Point out each leukocyte.
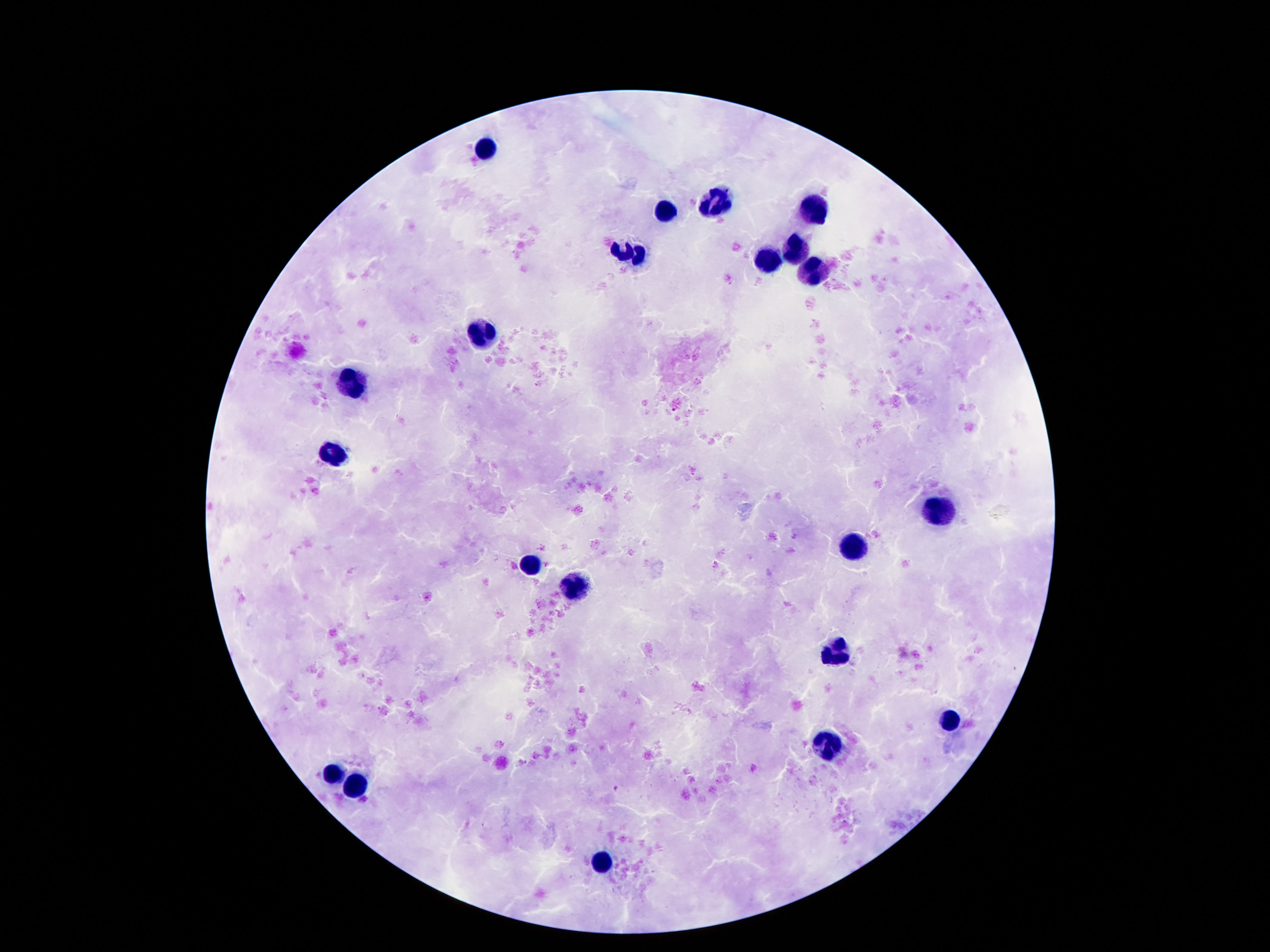

Approximate centers as (x, y) in pixels.
Leukocytes: (486, 148), (717, 204), (664, 211), (813, 213), (796, 246), (629, 251), (766, 258), (813, 274), (484, 333), (353, 382), (332, 456), (937, 510), (855, 545), (531, 562), (573, 587), (834, 654), (950, 721), (822, 743), (335, 774), (356, 785), (605, 862).

Giemsa stain. Thick peripheral-blood smear. Patient malaria status: not infected. 100x magnification. One field from this slide. Image is 1270×952 pixels. Smartphone photograph taken through the microscope eyepiece.